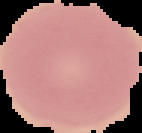
Summary:
  - Result: no malaria parasites detected
  - Image size: 142×133 pixels
  - Image type: cell region segmented out of the field of view; surrounding area masked to black
  - Preparation: thin blood smear